Name the parasite shown.
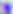

Toxoplasma gondii.

magnification = 400x
modality = micrograph